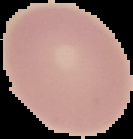
From a thin blood film. Segmented cell region on a black background. Malaria status: uninfected. Image is 133×139 pixels.